Outline platelets.
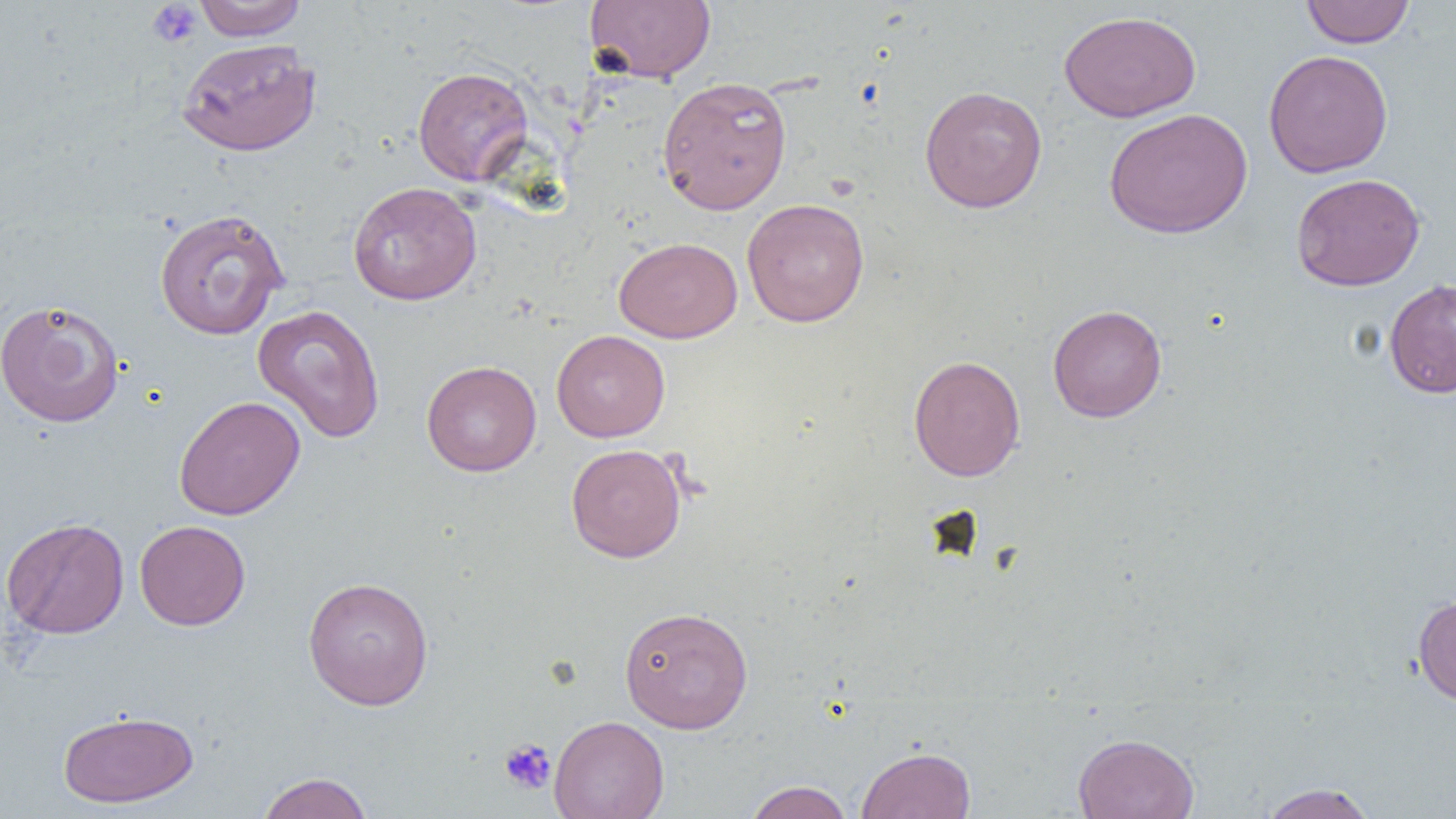

Approximate bounding boxes as (x1, y1, x2, y2) in pixels.
Platelets: (147, 1, 203, 48), (499, 738, 556, 795).

Uninfected red blood cell locations: (193, 0, 308, 41), (584, 0, 716, 84), (1300, 0, 1415, 48), (1058, 10, 1201, 122), (177, 39, 320, 156), (1263, 49, 1393, 178), (413, 66, 534, 187), (657, 76, 793, 215), (919, 85, 1048, 214), (1104, 108, 1253, 239), (1291, 173, 1425, 291), (348, 181, 482, 305), (741, 198, 870, 328), (153, 208, 289, 340), (614, 236, 742, 343), (1384, 278, 1456, 399), (0, 299, 125, 428), (252, 304, 385, 444), (1048, 304, 1167, 423), (552, 329, 670, 442), (908, 354, 1025, 482), (421, 360, 541, 477), (173, 396, 305, 520), (566, 443, 686, 562), (1, 517, 129, 639), (134, 519, 251, 630), (302, 576, 434, 710), (1413, 594, 1456, 706), (619, 606, 754, 733), (57, 709, 199, 808), (549, 714, 669, 819), (1073, 732, 1199, 819), (856, 746, 976, 819), (256, 772, 373, 819), (744, 780, 854, 819), (1258, 783, 1378, 819). Slide-level diagnosis: no evidence of blood parasites. Thin blood film. Optical microscopy. Single field of view. Image is 1456×819 pixels. Captured at 1000x magnification.